Classify this cell by malaria status.
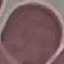
Uninfected.

Cell patch, automatically extracted from a larger field of view and resized to 64 × 64 pixels. Giemsa stain. Thin blood smear. Acquired by smartphone through the microscope eyepiece.